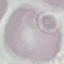

Summary:
  - Malaria status: uninfected
  - Capture: smartphone through the microscope eyepiece
  - Preparation: thin smear
  - Image type: automatically extracted cell patch, resized to 64 × 64 pixels
  - Stain: Giemsa